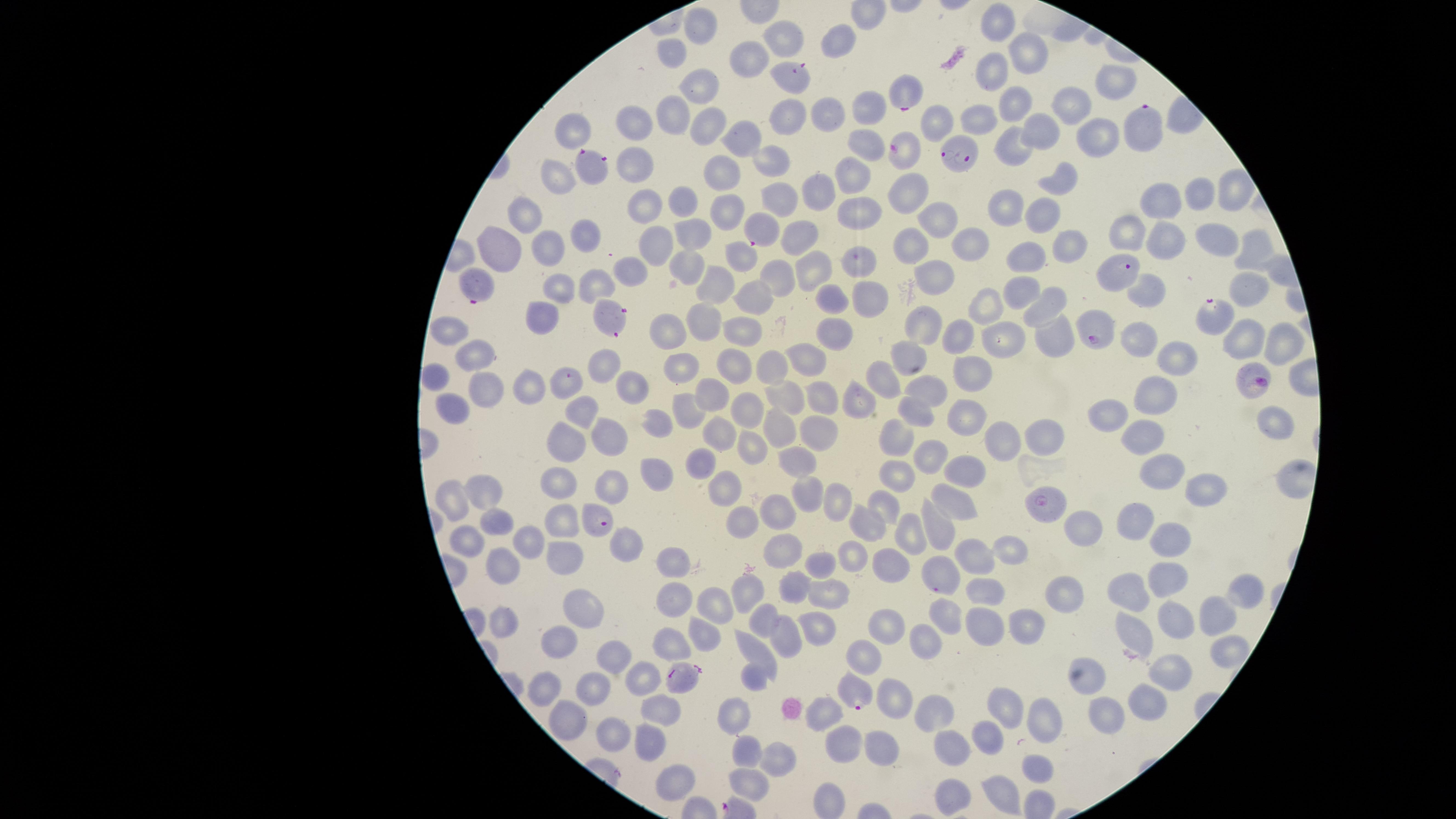
capture = smartphone photograph through the microscope eyepiece
preparation = thin blood smear
species = Plasmodium falciparum
visible region = circular
image size = 1456×819 pixels
parasitized RBCs = approximate marker points as (x, y) in pixels: (793, 77), (903, 92), (1139, 123), (902, 152), (960, 152), (592, 170), (760, 229), (1118, 272), (475, 281), (609, 312), (1218, 313), (1092, 325), (565, 382), (1254, 384), (1044, 506), (599, 521), (939, 578), (682, 676), (857, 690)
stain = Giemsa
field of view = single
presence = malaria parasites identified
uninfected RBCs = approximate marker points as (x, y) in pixels: (998, 23), (697, 31), (785, 36), (839, 48), (675, 52), (1030, 52), (750, 57), (992, 69), (1116, 81), (700, 87), (1012, 105), (1071, 105), (864, 109), (678, 113), (784, 115), (823, 115), (981, 116), (936, 123), (632, 124), (704, 127), (1046, 127), (575, 129), (1097, 137), (741, 139), (864, 144), (1011, 148), (775, 161), (636, 167), (563, 174), (720, 178), (851, 180), (1060, 181), (1229, 191), (822, 192), (908, 192), (1202, 193), (1163, 197), (783, 201), (682, 203), (647, 206), (1008, 206), (859, 209), (529, 210), (728, 212), (1037, 213), (938, 220), (1128, 230), (695, 232), (807, 233), (583, 236), (1167, 236), (1217, 237), (1067, 244), (908, 245), (657, 246), (551, 247), (963, 247), (1249, 249), (739, 251), (499, 256), (1026, 258), (861, 263), (689, 267), (627, 270), (813, 272), (781, 276), (939, 276), (559, 283), (594, 285), (715, 287), (1023, 290), (1147, 290), (1245, 290), (868, 297), (760, 298), (828, 299), (989, 305), (1046, 305), (543, 316), (704, 320), (922, 326), (668, 328), (742, 330), (451, 333), (831, 333), (1053, 336), (1138, 336), (954, 337), (1005, 337), (1244, 340), (1280, 340), (903, 351), (476, 355), (807, 355), (1178, 356), (606, 362), (735, 365), (771, 365), (675, 369), (971, 372), (433, 379), (529, 383), (630, 383), (879, 383), (483, 390), (929, 391), (825, 393), (1156, 394), (710, 396), (780, 401), (857, 401), (745, 408), (688, 409), (451, 410), (584, 410), (915, 414), (1272, 415), (964, 417), (1110, 417), (659, 420), (779, 429), (821, 431), (715, 434), (1047, 434), (615, 436), (1004, 438), (896, 439), (1143, 440), (568, 443), (757, 443), (930, 449), (697, 458), (799, 458), (1159, 466), (896, 468), (965, 470), (654, 471), (559, 479), (615, 481), (727, 486), (1205, 486), (483, 490), (803, 493), (450, 498), (833, 501), (953, 504), (885, 505), (776, 515), (565, 518), (747, 522), (868, 522), (501, 523), (932, 526), (1140, 526), (1088, 527), (905, 528), (467, 536), (625, 540), (1163, 540), (533, 545), (1009, 550), (785, 551), (855, 551), (568, 554), (978, 558), (675, 565), (822, 566), (887, 568), (502, 572), (1163, 575), (796, 584), (747, 587), (982, 589), (1238, 590), (1128, 591), (832, 593), (1067, 593), (669, 601), (721, 603), (583, 604), (765, 618), (947, 619), (1172, 620), (1214, 620), (508, 622), (1015, 622), (892, 626), (817, 627), (977, 627), (1133, 631), (705, 633), (667, 636), (564, 640), (923, 640), (786, 641), (1218, 650), (759, 652), (864, 655), (618, 657), (756, 675), (1175, 676), (639, 678), (1092, 680), (548, 686), (597, 689), (890, 694), (1147, 700), (1007, 704), (661, 708), (737, 711), (819, 711), (936, 711), (1110, 717), (573, 721), (1045, 721), (988, 734), (609, 736), (645, 741), (952, 744), (842, 747), (877, 748), (750, 750), (779, 754), (1037, 769), (674, 780), (751, 780), (954, 788), (1003, 794)